Assess the morphology of the erythrocytes.
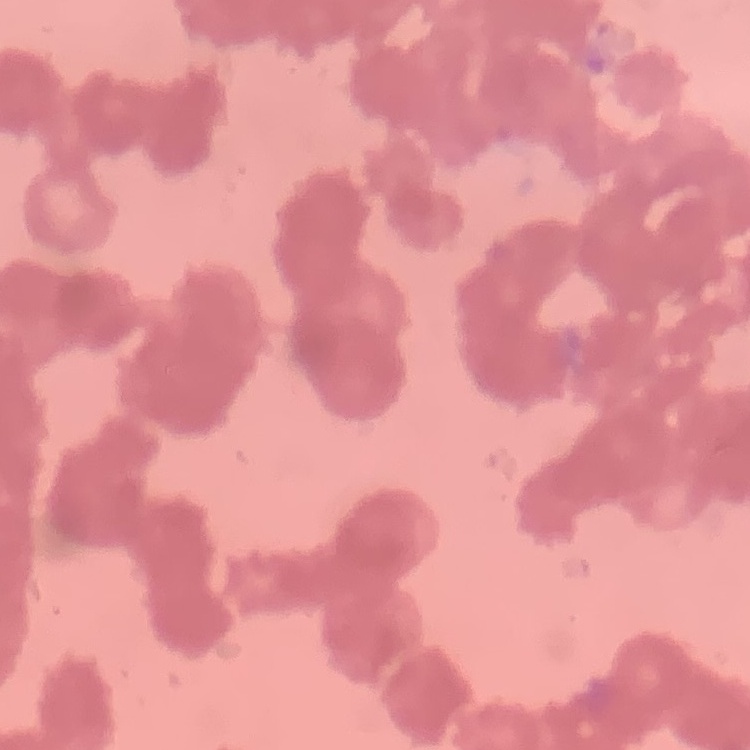
Rouleaux formation.

Stained with either Field's or Giemsa. Thin blood smear. Square crop of a larger photomicrograph.